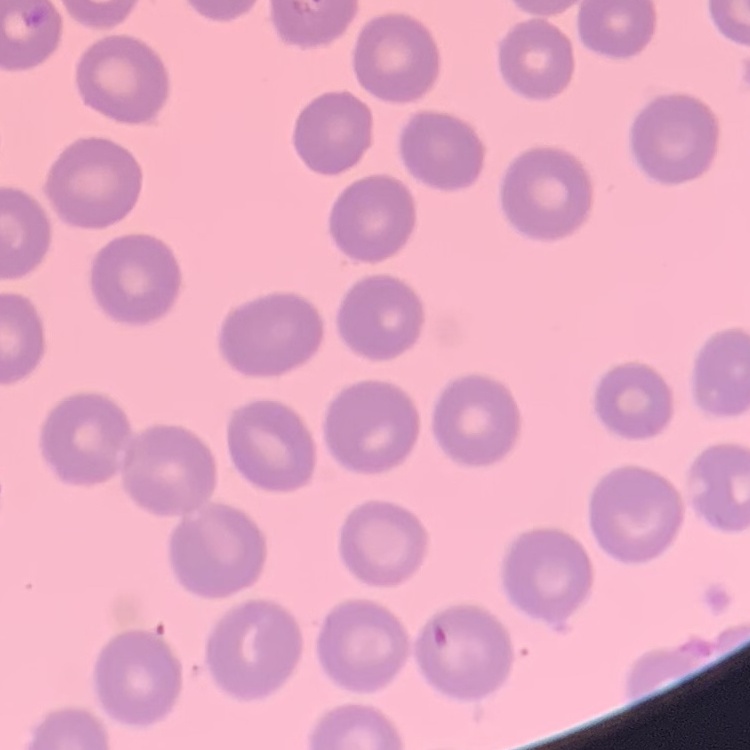

red blood cell morphology = no rouleaux formation
image type = square crop of a larger photomicrograph
preparation = thin peripheral smear
stain = Field's or Giemsa